Assess this cell for malaria.
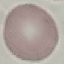

It is uninfected.

image_type: cell patch, automatically extracted from a larger field of view and resized to 64 × 64 pixels
preparation: thin blood film
stain: Giemsa
capture: smartphone through the microscope eyepiece